Report the malaria status of this cell.
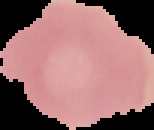

It is uninfected.

image size = 154×130 pixels
preparation = thin blood smear
image type = segmented cell region with the area outside set to black